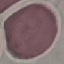

result = no malaria parasites seen
capture = smartphone camera at the microscope eyepiece
image type = cell patch, automatically extracted from a larger field of view and resized to 64 × 64 pixels
preparation = thin blood film
stain = Giemsa